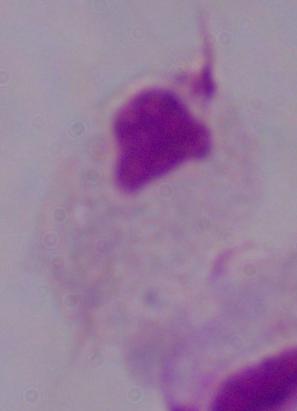
magnification: 1000x
identification: trichomonad
modality: photomicrograph